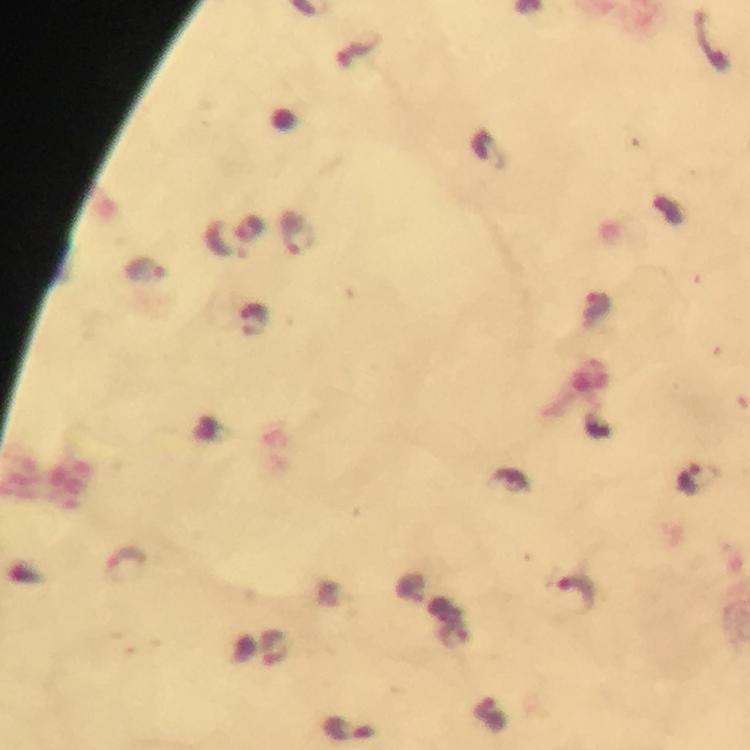
Plasmodium parasite locations = approximate centers as {x, y} in pixels: {297, 232}, {223, 241}, {143, 271}, {597, 303}, {693, 479}, {127, 561}, {573, 592}, {272, 646}, {348, 729}
preparation = thick blood film
context = from a diagnostic examination for malaria
immersion oil = applied
cropped from = one field of view
stain = Giemsa
image size = 750×750 pixels
magnification = 100x
capture = smartphone mounted on the microscope